Name the blood parasite species.
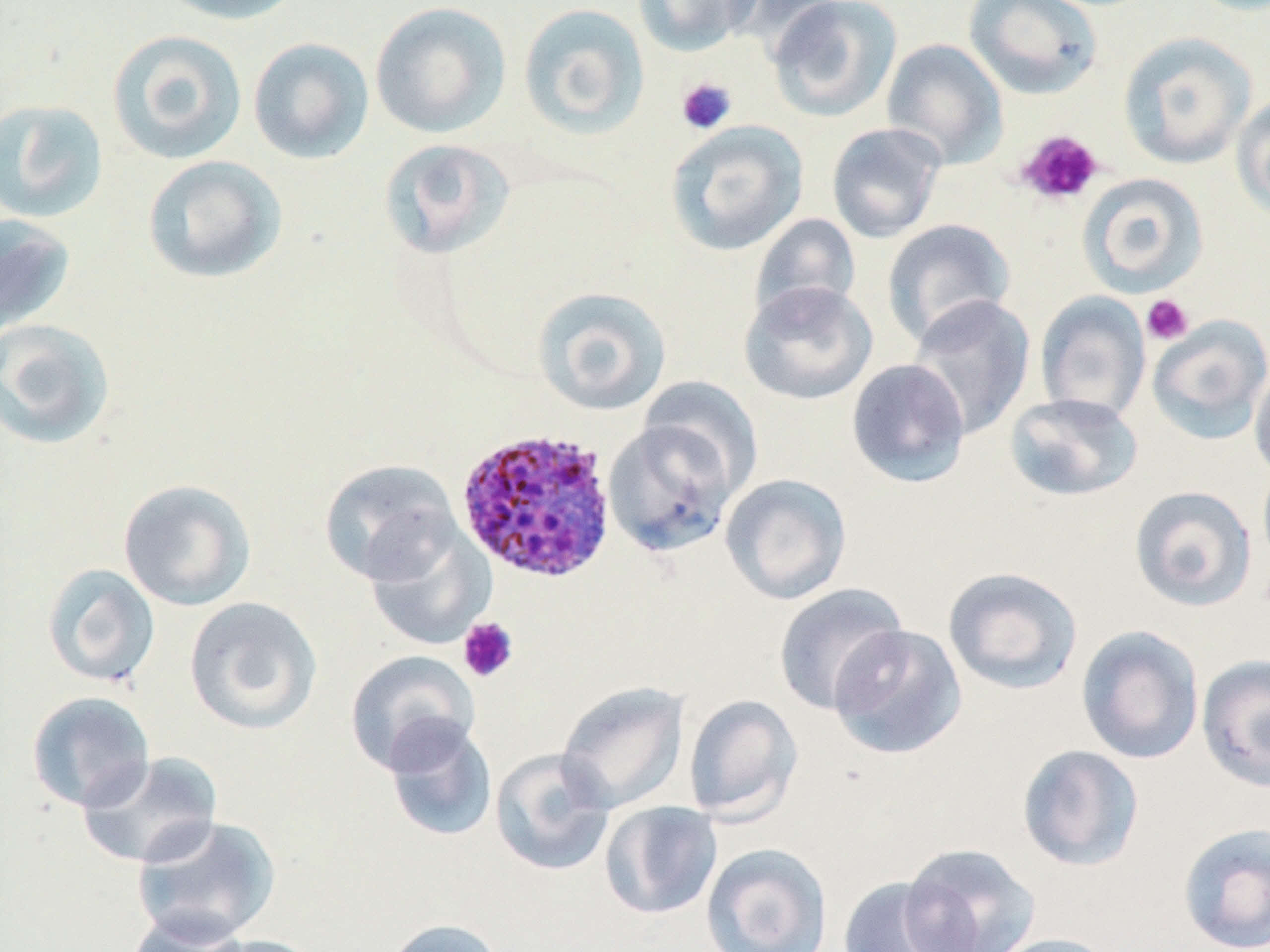
Plasmodium ovale.

Approximate bounding boxes as (x1,y1)-(x2,y2) corner pairs in pixels. Platelet locations: (676,77)-(737,135), (1015,129)-(1104,206), (1141,294)-(1194,346), (457,616)-(519,683). Uninfected red blood cell locations: (155,0)-(307,26), (632,0)-(762,57), (719,0)-(849,54), (963,0)-(1103,101), (370,1)-(511,139), (767,1)-(902,122), (517,2)-(650,140), (107,29)-(248,165), (1117,31)-(1256,169), (248,37)-(375,164), (881,38)-(1008,169), (1231,92)-(1270,221), (0,99)-(109,223), (665,120)-(809,256), (826,122)-(947,244), (379,138)-(515,259), (142,155)-(287,284), (1077,172)-(1209,296), (749,213)-(862,326), (0,215)-(76,337), (881,218)-(1016,348), (739,280)-(878,406), (531,286)-(672,415), (1035,292)-(1151,424), (907,294)-(1036,440), (1146,314)-(1270,445), (0,318)-(116,451), (845,358)-(971,489), (1249,361)-(1270,483), (638,377)-(763,495), (1004,392)-(1144,502), (603,416)-(742,558), (319,459)-(461,586), (720,473)-(852,605), (118,478)-(256,611), (1129,485)-(1258,612), (364,524)-(495,650), (42,563)-(160,688), (942,566)-(1083,695), (773,582)-(910,715), (184,596)-(323,735), (828,623)-(968,760), (1075,625)-(1205,765), (345,649)-(480,775), (1196,653)-(1270,792), (556,680)-(690,814), (25,690)-(156,813), (683,693)-(803,823), (382,717)-(498,843), (1016,744)-(1145,871), (490,747)-(615,877), (76,751)-(224,869), (599,801)-(723,920), (130,814)-(281,946), (1176,821)-(1270,952), (897,842)-(1040,952), (701,843)-(832,952), (835,876)-(974,952), (127,912)-(252,952), (383,918)-(506,952), (985,933)-(1124,952), (198,934)-(329,952). Plasmodium ovale-infected red blood cell locations: (454,426)-(618,584). Image is 1270×952 pixels. One field of a larger specimen. Captured at 1000x magnification. Thin blood film. May-Grünwald-Giemsa-stained preparation. Optical microscopy.